Classify this cell by malaria status.
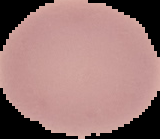

It is uninfected.

{
  "image_type": "segmented cell region on a black background",
  "image_size": "160×139 pixels",
  "preparation": "thin blood smear"
}